Classify this cell by malaria status.
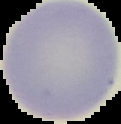
It is uninfected.

image size = 121×124 pixels
preparation = thin blood smear
image type = segmented cell region with the area outside set to black